Identify the cell.
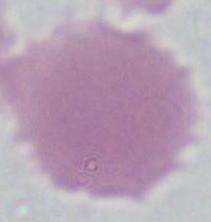

An erythrocyte.

Summary:
  - Modality: micrograph
  - Magnification: 1000x